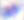 Toxoplasma gondii is seen. Photomicrograph. Captured at 400x magnification.